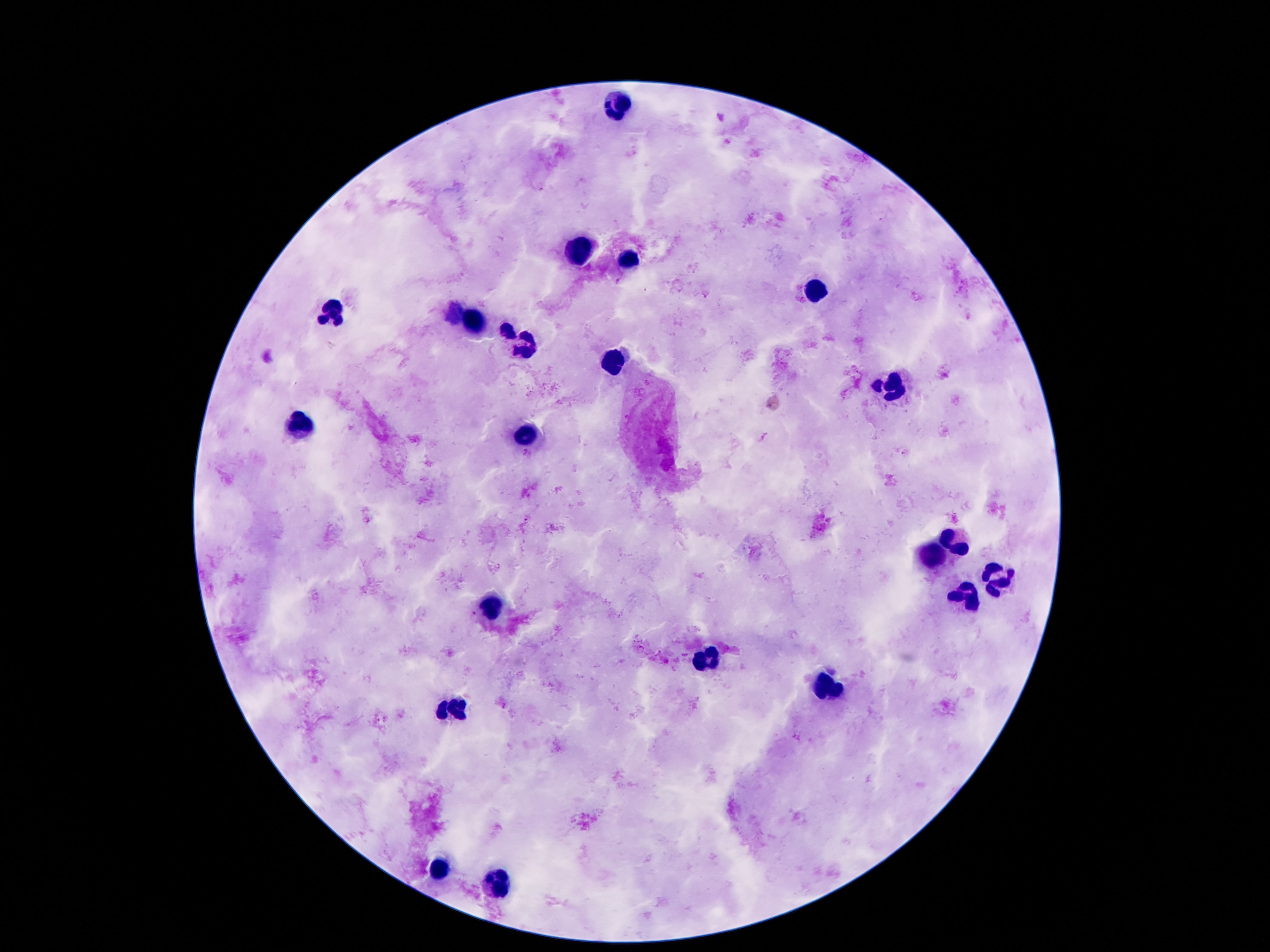

Approximate centers as [x, y] in pixels. Leukocyte locations: [618, 102], [580, 249], [629, 255], [812, 293], [329, 311], [474, 322], [523, 348], [613, 362], [890, 385], [302, 426], [530, 435], [956, 540], [932, 556], [998, 578], [967, 596], [494, 604], [708, 660], [828, 687], [455, 707], [439, 869], [497, 882]. Thick peripheral-blood smear. 100x magnification. Image is 1270×952 pixels. Single field of view. Patient malaria status: not infected. Giemsa stain. Photographed through the microscope eyepiece with a smartphone camera.